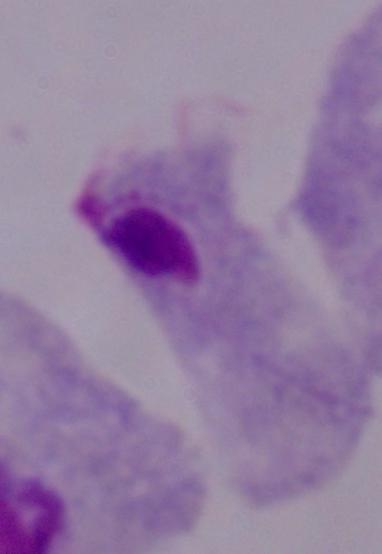
Captured at 1000x magnification. Photomicrograph. A trichomonad is shown.